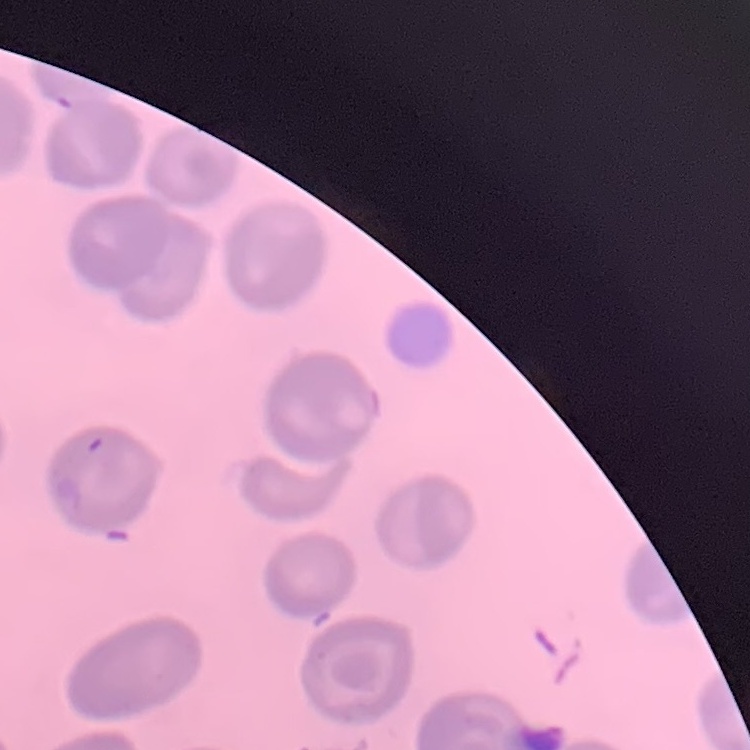
The erythrocytes exhibit no rouleaux formation. Stained with either Field's or Giemsa. Thin blood smear. One tile cut from a larger photomicrograph.